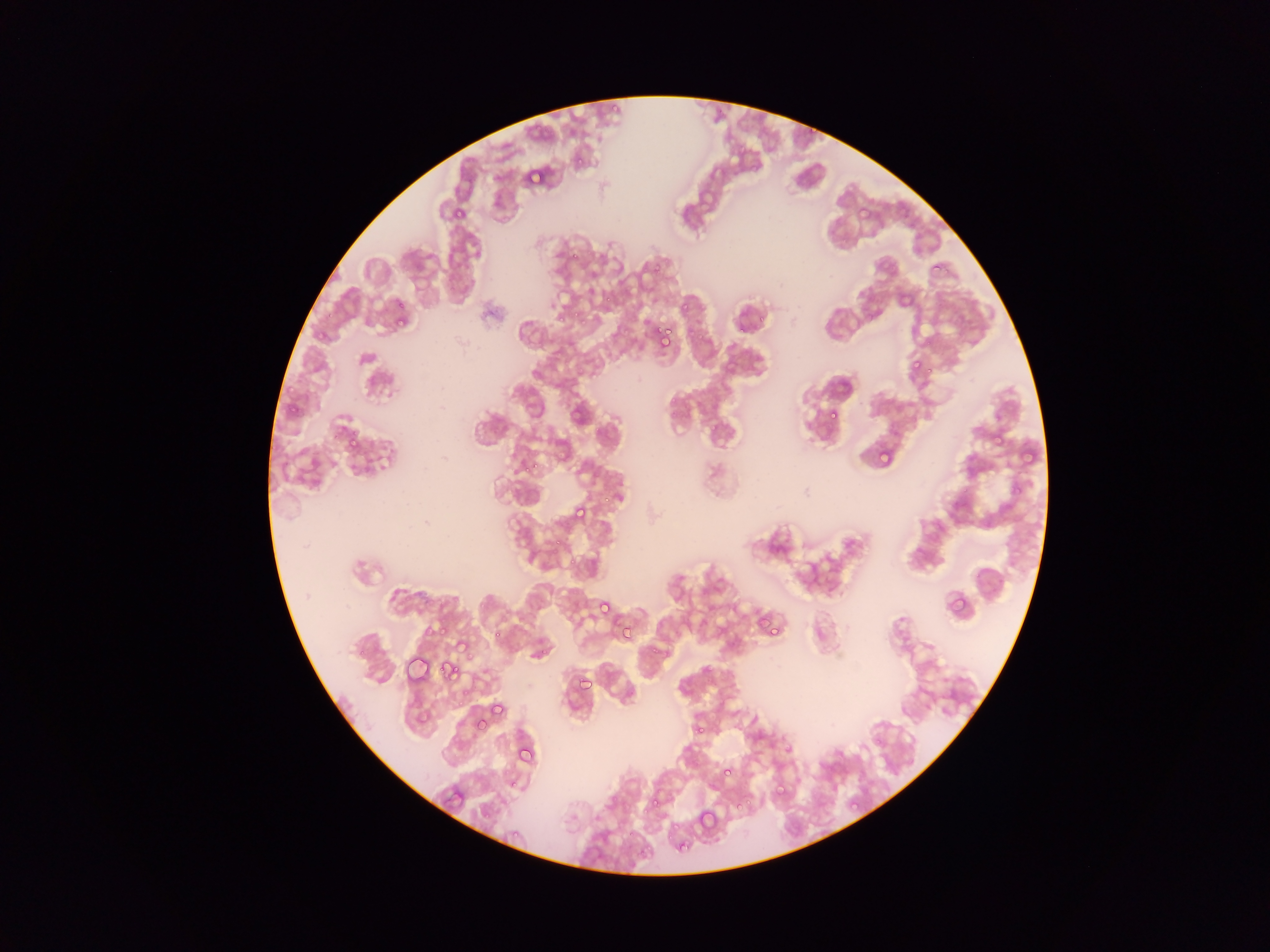

capture: mobile-phone photograph through a microscope
country: Ghana
field_of_view: single
image_size: 1270×952 pixels
plasmodium_parasite_locations: 'approximate bounding boxes as left top right bottom in pixels: 612 101 621 112; 807 128 818 134; 576 156 584 167; 750 161 761 173; 528 164 545 178; 525 167 543 185; 455 208 463 216; 570 253 578 261; 652 261 662 275; 932 263 941 270; 605 293 613 305; 897 293 909 305; 394 298 404 308; 681 300 689 309; 329 308 340 318; 572 312 580 318; 757 314 767 326; 395 315 406 325; 579 317 589 327; 736 324 747 336; 652 327 666 340; 666 329 674 335; 697 332 704 342; 663 339 673 346; 909 358 922 373; 926 367 940 379; 286 401 295 412; 828 409 839 420; 992 412 1006 428; 993 428 1006 442; 347 431 359 446; 876 447 892 463; 532 461 541 474; 1012 484 1022 496; 962 486 968 496; 601 495 613 505; 572 504 589 522; 554 539 563 547; 569 556 581 565; 945 592 965 612; 479 597 488 610; 595 599 611 615; 616 619 634 636; 431 620 453 643; 758 620 767 628; 621 625 634 637; 765 626 778 637; 494 629 505 640; 538 647 550 657; 650 648 658 656; 467 651 477 660; 439 661 458 680; 705 665 714 673; 576 675 590 691; 463 684 474 698; 493 700 503 716; 474 715 487 727; 694 723 708 737; 875 735 883 746; 520 749 537 762; 723 769 731 778; 512 778 520 789; 775 786 785 798; 746 795 754 806; 651 797 660 805; 847 798 857 809; 483 803 495 820; 733 803 744 813; 641 806 653 815; 696 808 716 829; 674 821 681 831; 630 823 639 837; 511 829 518 839; 664 836 673 841; 679 842 689 853; 638 850 648 858 | approximate x y pixel centers of objects too small to bound: 560 317; 525 470'
preparation: thin blood smear